Give the extent of all Plasmodium malariae-infected red blood cells.
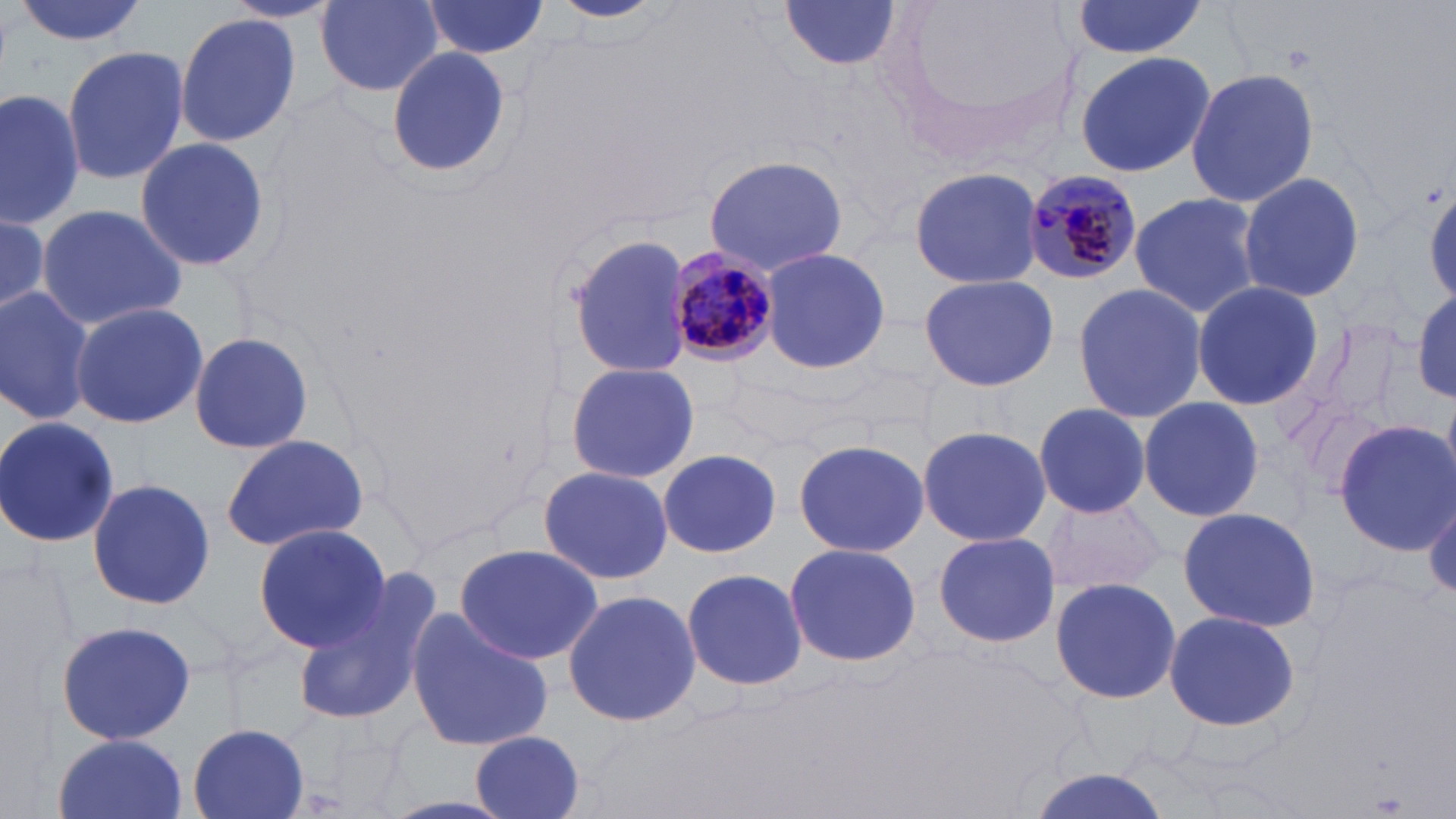

Approximate bounding boxes as [x1, y1, x2, y2] in pixels.
Plasmodium malariae-infected red blood cells: [1020, 168, 1142, 286], [666, 251, 780, 367].

slide-level diagnosis = Plasmodium malariae
magnification = 1000x
stain = May-Grünwald-Giemsa
image size = 1456×819 pixels
uninfected red blood cell locations = approximate bounding boxes as [x1, y1, x2, y2] in pixels: [12, 0, 152, 47], [316, 0, 445, 94], [549, 0, 667, 24], [778, 0, 904, 75], [877, 0, 1091, 169], [420, 1, 550, 59], [1068, 2, 1209, 58], [176, 12, 301, 145], [63, 46, 189, 183], [384, 46, 511, 178], [1073, 51, 1214, 178], [1185, 67, 1319, 211], [0, 87, 83, 230], [133, 134, 272, 274], [701, 154, 848, 274], [908, 167, 1043, 288], [1237, 170, 1365, 306], [1129, 191, 1260, 322], [35, 203, 190, 328], [0, 213, 52, 324], [565, 233, 693, 380], [761, 245, 892, 377], [917, 271, 1060, 391], [1189, 279, 1323, 413], [1070, 281, 1208, 425], [0, 285, 95, 426], [1410, 286, 1456, 408], [68, 301, 207, 429], [188, 331, 314, 456], [563, 360, 699, 485], [1138, 394, 1263, 522], [1033, 402, 1152, 519], [0, 416, 119, 548], [1332, 418, 1455, 554], [917, 424, 1053, 548], [220, 433, 370, 553], [791, 439, 930, 557], [657, 447, 782, 559], [537, 465, 672, 586], [86, 479, 217, 611], [1040, 493, 1166, 598], [1427, 493, 1456, 600], [1176, 506, 1321, 631], [251, 524, 390, 652], [930, 533, 1065, 648], [783, 541, 920, 669], [453, 544, 604, 666], [681, 566, 807, 691], [1050, 575, 1183, 706], [561, 589, 702, 727], [293, 593, 432, 726], [404, 608, 553, 753], [1162, 608, 1301, 734], [53, 620, 200, 747], [188, 724, 309, 819], [470, 732, 588, 819], [51, 735, 191, 819], [1025, 769, 1174, 819]
field of view = one of a larger specimen
preparation = thin blood film
modality = light microscopy